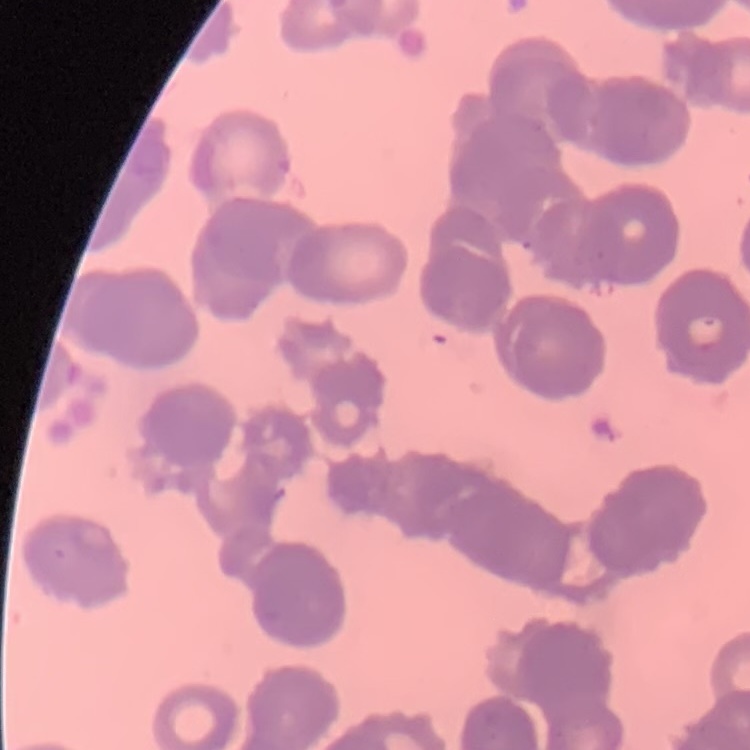 The red blood cells show rouleaux formation. Stained with either Field's or Giemsa. One tile cut from a larger photomicrograph. Thin peripheral smear.